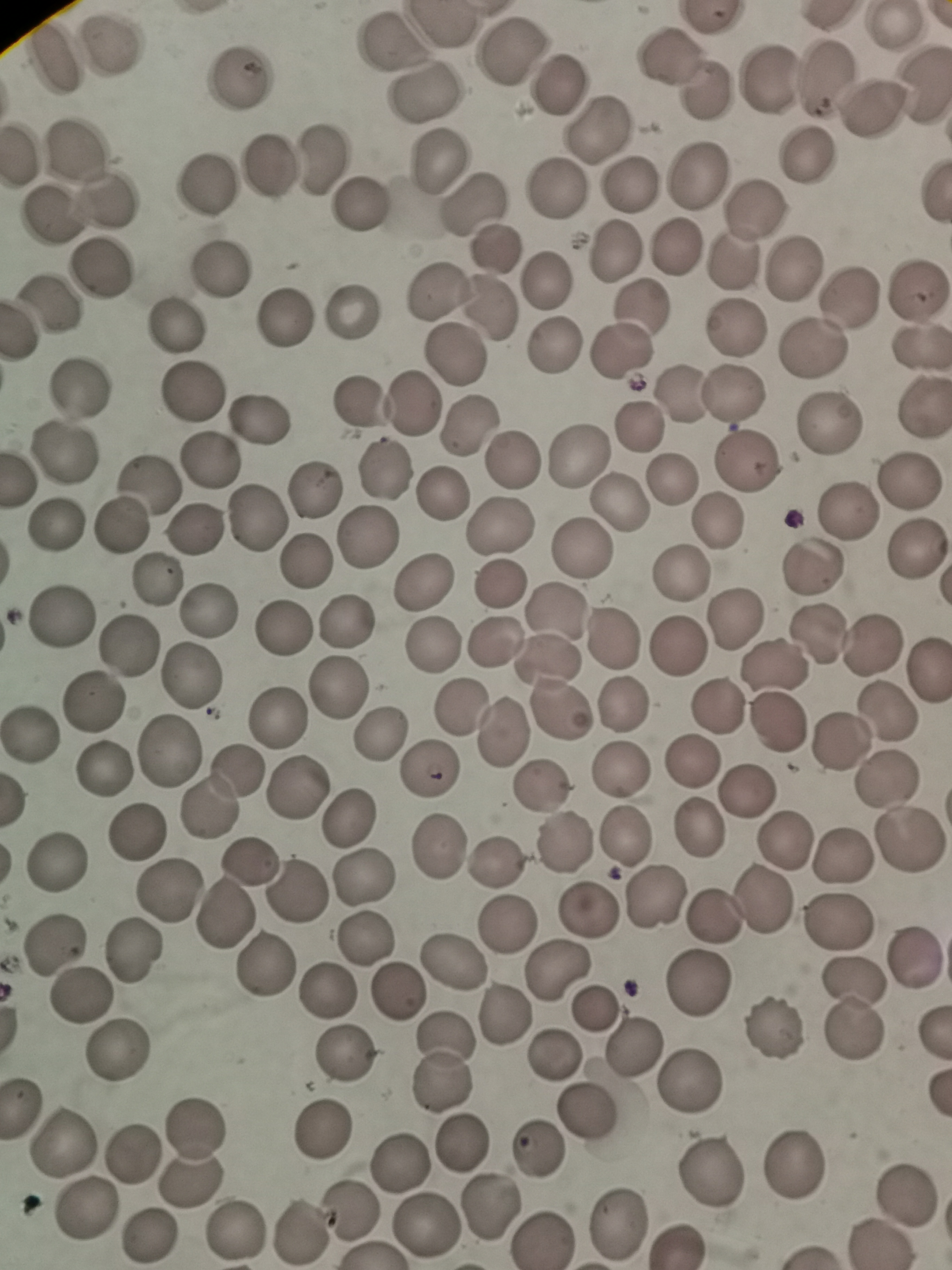

Approximate object centers, in pixels from the top-left corner. Cell locations: (x=897, y=29), (x=112, y=41), (x=388, y=45), (x=512, y=49), (x=668, y=54), (x=55, y=56), (x=825, y=76), (x=241, y=78), (x=765, y=78), (x=924, y=82), (x=558, y=84), (x=708, y=89), (x=427, y=94), (x=875, y=108), (x=598, y=129), (x=75, y=145), (x=17, y=152), (x=323, y=154), (x=805, y=155), (x=437, y=162), (x=270, y=168), (x=697, y=172), (x=207, y=182), (x=632, y=182), (x=554, y=190), (x=107, y=201), (x=363, y=203), (x=472, y=205), (x=754, y=209), (x=50, y=217), (x=676, y=246), (x=496, y=249), (x=613, y=250), (x=731, y=261), (x=794, y=265), (x=223, y=268), (x=101, y=272), (x=543, y=281), (x=438, y=291), (x=916, y=292), (x=848, y=297), (x=50, y=303), (x=642, y=307), (x=489, y=309), (x=352, y=312), (x=285, y=317), (x=175, y=329), (x=736, y=330), (x=555, y=346), (x=815, y=348), (x=622, y=351), (x=916, y=351), (x=455, y=355), (x=80, y=387), (x=194, y=393), (x=733, y=393), (x=682, y=397), (x=361, y=403), (x=413, y=403), (x=922, y=410), (x=260, y=420), (x=830, y=423), (x=468, y=425), (x=638, y=426), (x=63, y=455), (x=581, y=456), (x=210, y=461), (x=511, y=461), (x=745, y=461), (x=386, y=470), (x=669, y=479), (x=911, y=480), (x=148, y=481), (x=313, y=486), (x=443, y=495), (x=622, y=503), (x=852, y=510), (x=257, y=519), (x=719, y=521), (x=56, y=524), (x=122, y=526), (x=196, y=526), (x=499, y=527), (x=366, y=539), (x=581, y=549), (x=915, y=551), (x=305, y=562), (x=813, y=565), (x=681, y=574), (x=160, y=580), (x=423, y=582), (x=500, y=583), (x=210, y=610), (x=62, y=616), (x=734, y=619), (x=344, y=624), (x=283, y=629), (x=814, y=633), (x=493, y=640), (x=614, y=640), (x=874, y=643), (x=128, y=645), (x=433, y=645), (x=678, y=645), (x=552, y=659), (x=773, y=670), (x=930, y=671), (x=189, y=677), (x=337, y=688), (x=93, y=700), (x=621, y=705), (x=717, y=707), (x=464, y=709), (x=887, y=713), (x=277, y=716), (x=777, y=723), (x=506, y=731), (x=32, y=734), (x=382, y=736), (x=841, y=741), (x=169, y=749), (x=692, y=762), (x=235, y=768), (x=107, y=770), (x=431, y=770), (x=622, y=770), (x=886, y=780), (x=298, y=787), (x=539, y=788), (x=748, y=793), (x=208, y=809), (x=351, y=816), (x=136, y=832), (x=627, y=837), (x=785, y=839), (x=908, y=842), (x=566, y=843), (x=438, y=846), (x=842, y=854), (x=56, y=862), (x=498, y=863), (x=250, y=864), (x=366, y=878), (x=169, y=890), (x=297, y=893), (x=657, y=898), (x=766, y=899), (x=589, y=911), (x=228, y=913), (x=712, y=917), (x=507, y=923), (x=835, y=923), (x=367, y=939), (x=55, y=943), (x=913, y=952), (x=132, y=954), (x=451, y=961), (x=264, y=965), (x=562, y=970), (x=852, y=982), (x=698, y=985), (x=324, y=990), (x=395, y=991), (x=84, y=997), (x=596, y=1009), (x=502, y=1013), (x=854, y=1025), (x=778, y=1027), (x=630, y=1047), (x=342, y=1051), (x=120, y=1054), (x=553, y=1054), (x=442, y=1066), (x=690, y=1084), (x=23, y=1107), (x=589, y=1114), (x=325, y=1127), (x=465, y=1144), (x=64, y=1145), (x=192, y=1150), (x=540, y=1150), (x=134, y=1152), (x=402, y=1162), (x=801, y=1164), (x=710, y=1171), (x=903, y=1194), (x=494, y=1204), (x=84, y=1207), (x=353, y=1212), (x=426, y=1226), (x=617, y=1226), (x=235, y=1232), (x=302, y=1232), (x=153, y=1234), (x=542, y=1238). Giemsa stain. Thin blood smear. Image is 952×1270 pixels. Single field of view. Photographed with a smartphone camera at the microscope eyepiece.